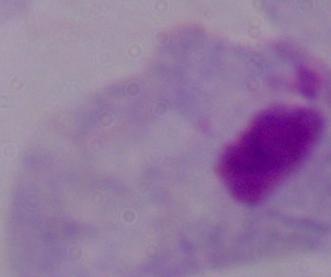

magnification = 1000x
identification = trichomonad
modality = micrograph